Identify the parasite.
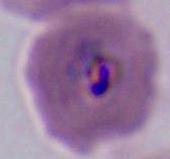

This is Plasmodium.

magnification = 400x or 1000x
modality = photomicrograph